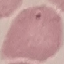

Malaria status: uninfected. Automatically extracted cell patch, resized to 64 × 64 pixels. Photographed with a smartphone camera at the microscope eyepiece. Giemsa-stained preparation. Thin smear of blood.